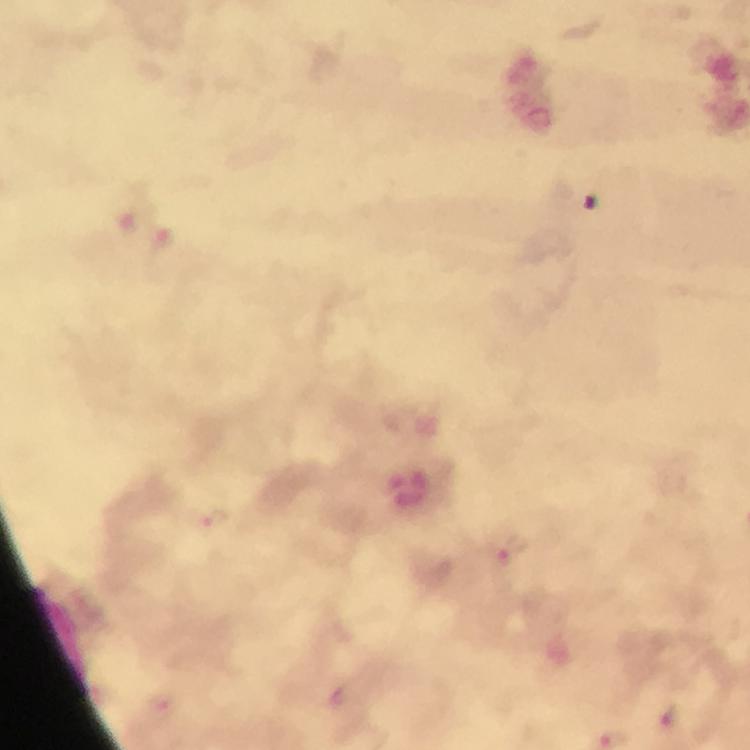
Approximate centers as [x, y] in pixels. Plasmodium parasite locations: [215, 521], [497, 555], [668, 716]. Cropped region of a single field of view. Immersion oil was used. From a malaria diagnostic workup. Photographed through the microscope with a smartphone camera. Giemsa stain. Thick blood smear. At 100x magnification. Image is 750×750 pixels.